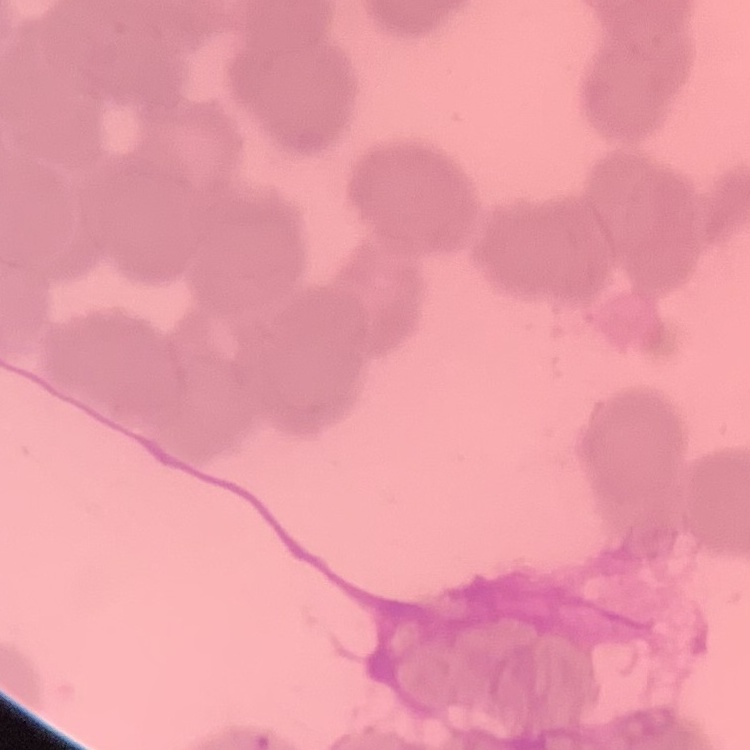

red blood cell morphology = rouleaux formation
image type = one tile cut from a larger photomicrograph
preparation = thin blood smear
stain = Field's or Giemsa